Report the malaria status.
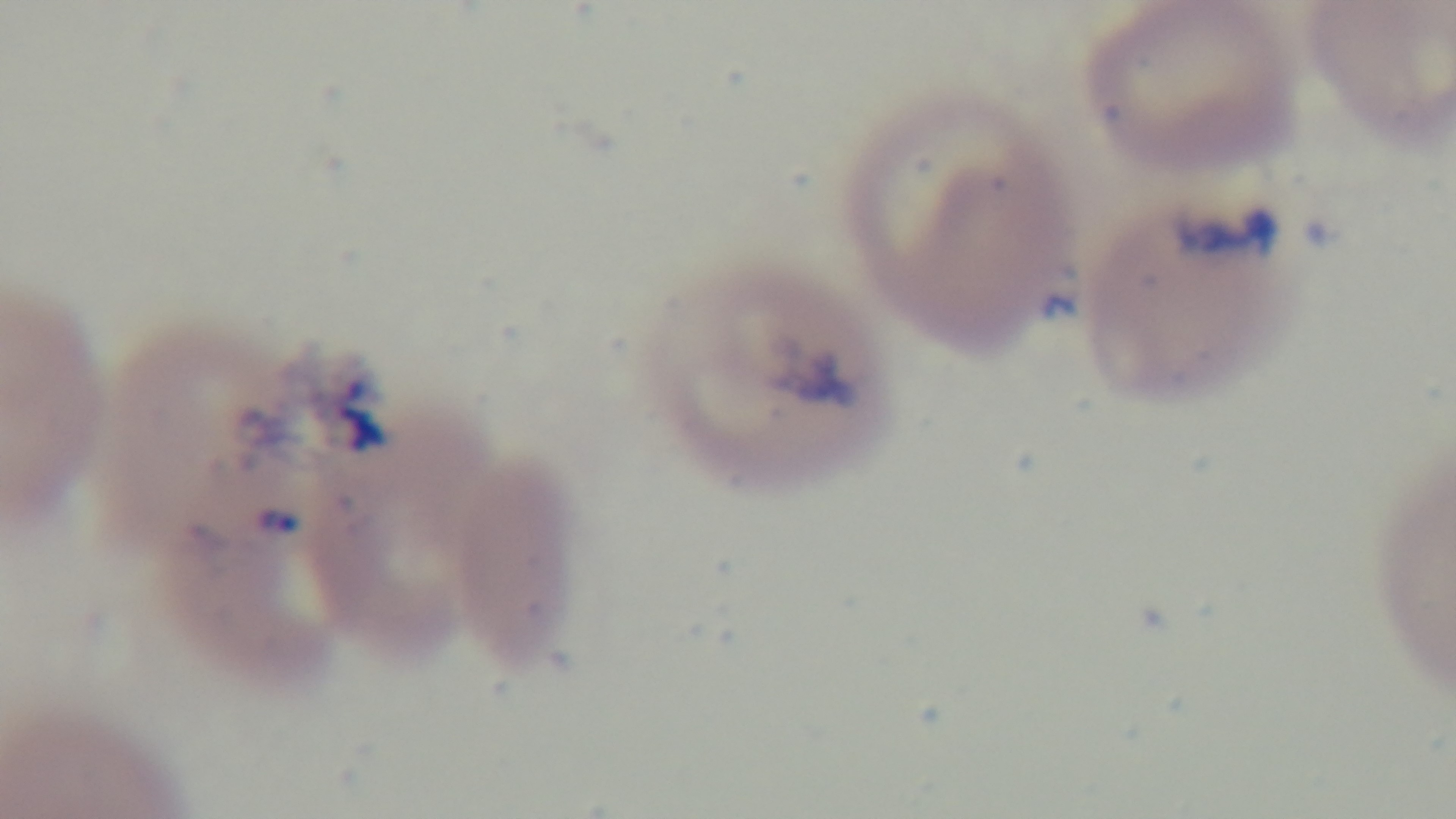
It is infected.

Summary:
  - Objective: 100x oil immersion
  - Capture: mounted 4K digital camera
  - Preparation: thin blood film
  - Stain: Giemsa
  - Field of view: single
  - Modality: light microscopy